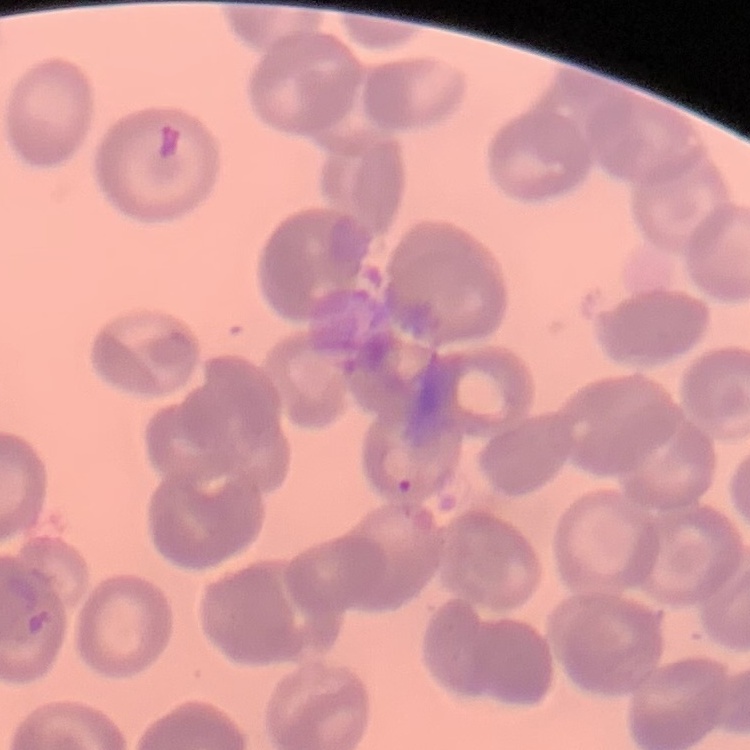

The red blood cells show no rouleaux formation. One tile cut from a larger photomicrograph. Thin peripheral smear. Field's or Giemsa stain.